Give the extent of all Plasmodium falciparum-infected red blood cells.
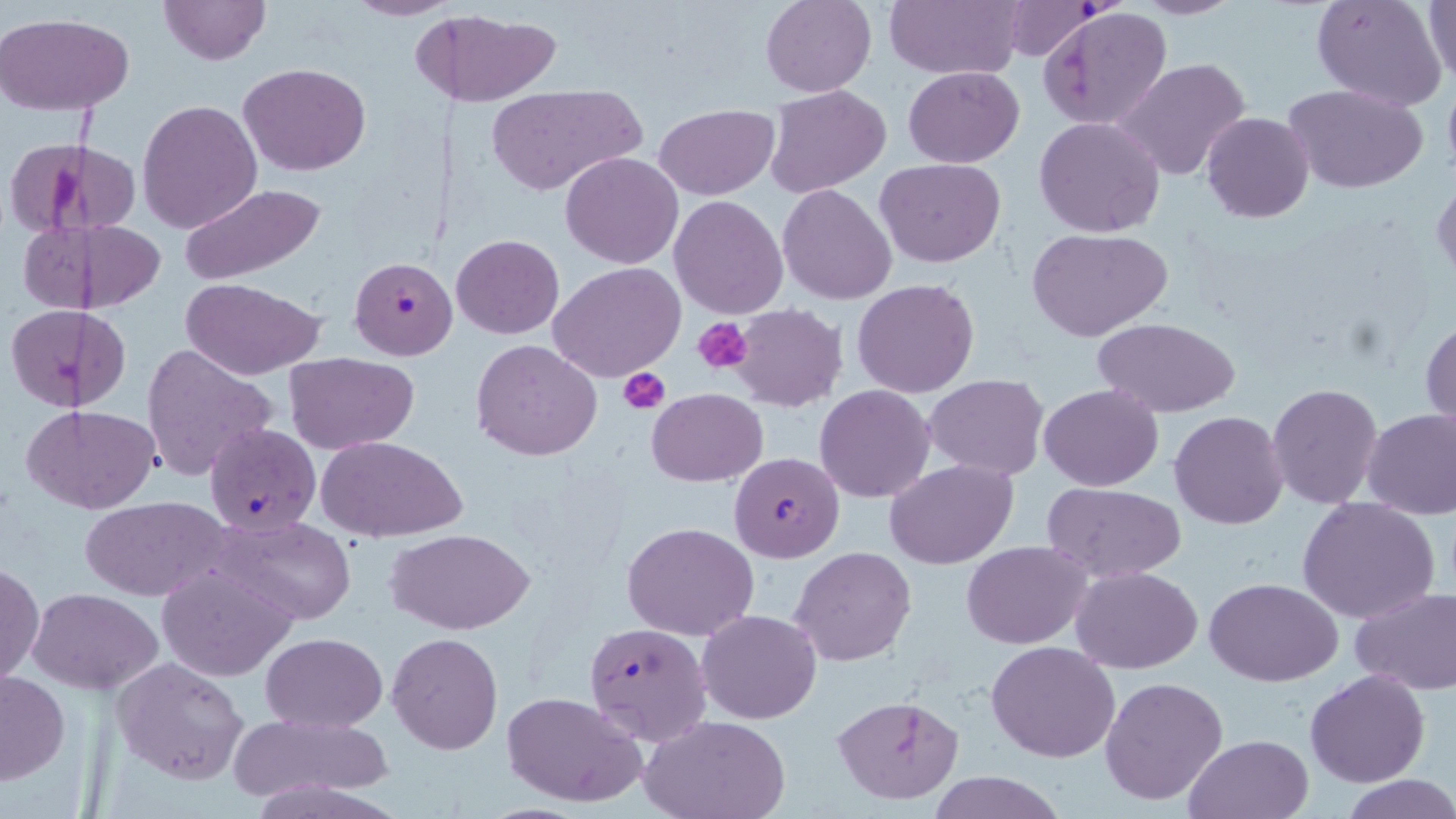
Approximate bounding boxes as [x1, y1, x2, y2] in pixels.
Plasmodium falciparum-infected red blood cells: [1001, 0, 1100, 62], [349, 253, 459, 361], [205, 423, 320, 535], [730, 452, 843, 562], [583, 621, 713, 747].

Uninfected red blood cell locations: [159, 0, 269, 65], [760, 0, 876, 96], [885, 0, 1022, 80], [1132, 0, 1244, 19], [1311, 0, 1448, 112], [347, 1, 455, 21], [1422, 1, 1456, 84], [1033, 6, 1165, 128], [446, 11, 563, 108], [0, 13, 136, 116], [410, 15, 455, 105], [1113, 57, 1252, 180], [238, 62, 370, 176], [903, 66, 1024, 167], [1442, 79, 1456, 185], [486, 84, 643, 195], [1284, 84, 1429, 196], [767, 86, 892, 198], [137, 99, 263, 233], [654, 104, 777, 198], [1202, 112, 1315, 223], [1033, 116, 1166, 238], [4, 140, 97, 238], [41, 142, 142, 237], [561, 151, 684, 268], [875, 159, 1006, 268], [1432, 180, 1455, 283], [178, 181, 328, 286], [777, 184, 896, 305], [670, 194, 788, 319], [83, 219, 166, 312], [17, 220, 86, 313], [1027, 227, 1173, 341], [451, 233, 564, 339], [549, 262, 686, 381], [178, 277, 329, 381], [852, 279, 980, 399], [732, 304, 847, 412], [6, 306, 82, 411], [75, 309, 129, 408], [1093, 317, 1240, 419], [1422, 318, 1455, 429], [471, 339, 603, 460], [142, 343, 278, 480], [285, 352, 418, 453], [924, 373, 1049, 478], [1039, 383, 1164, 491], [1266, 383, 1383, 509], [814, 384, 935, 504], [647, 388, 765, 486], [26, 404, 160, 514], [1362, 407, 1456, 521], [1171, 411, 1288, 529], [316, 434, 467, 541], [885, 459, 1019, 570], [1043, 483, 1187, 582], [81, 496, 230, 602], [1298, 496, 1442, 624], [207, 514, 359, 624], [623, 521, 760, 640], [387, 529, 533, 635], [962, 540, 1093, 649], [790, 546, 916, 666], [1, 561, 43, 691], [158, 563, 298, 680], [1072, 566, 1202, 673], [1205, 576, 1344, 686], [29, 587, 163, 694], [1349, 587, 1456, 694], [697, 609, 822, 724], [261, 632, 388, 732], [388, 632, 503, 753], [988, 641, 1120, 764], [111, 658, 250, 785], [1, 668, 68, 789], [1306, 670, 1431, 787], [1099, 676, 1229, 806], [501, 690, 648, 809], [832, 694, 965, 804], [231, 713, 392, 806], [643, 714, 790, 819], [1183, 735, 1314, 819], [928, 770, 1065, 819], [1341, 776, 1456, 818]. Platelet locations: [694, 317, 754, 375], [618, 367, 671, 413]. Slide-level diagnosis: Plasmodium falciparum. Image is 1456×819 pixels. One field of a larger specimen. 1000x magnification. Light microscopy. May-Grünwald-Giemsa-stained preparation. Thin blood film.